Name the parasite shown.
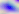
Toxoplasma gondii.

modality = micrograph
magnification = 400x